Assess this cell for malaria.
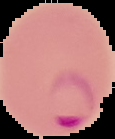

It is parasitized.

From a thin blood film. Image is 115×139 pixels. Segmented cell region on a black background.